Name the cell type shown.
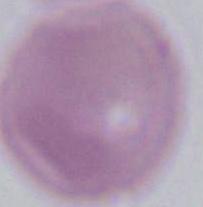

This is an erythrocyte.

Summary:
  - Magnification: 1000x
  - Modality: photomicrograph